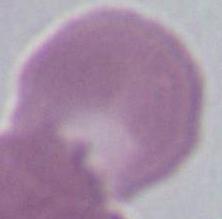
Photomicrograph. An erythrocyte is seen. Captured at 1000x magnification.